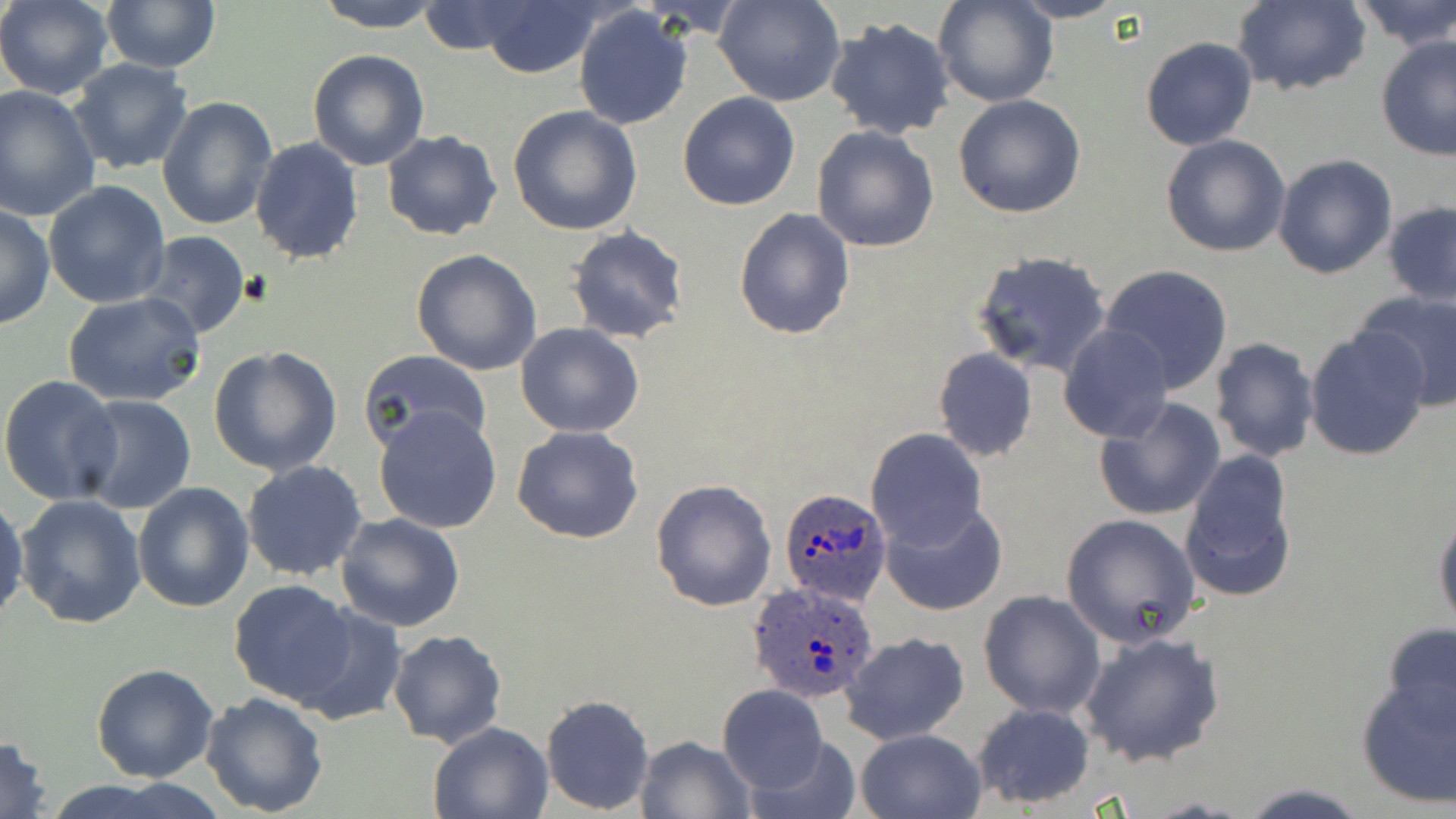
{
  "slide_level_diagnosis": "Plasmodium ovale",
  "image_size": "1456×819 pixels",
  "modality": "light microscopy",
  "field_of_view": "single",
  "magnification": "1000x",
  "preparation": "thin blood film",
  "stain": "May-Grünwald-Giemsa",
  "uninfected_red_blood_cell_locations": "approximate bounding boxes as [x1, y1, x2, y2] in pixels: [0, 0, 114, 99], [100, 0, 220, 72], [314, 0, 444, 32], [716, 0, 843, 106], [934, 0, 1055, 107], [1008, 0, 1126, 23], [1348, 0, 1456, 49], [473, 1, 604, 79], [1231, 1, 1370, 96], [418, 2, 525, 55], [572, 4, 693, 130], [824, 16, 956, 140], [1376, 33, 1456, 160], [1139, 37, 1258, 152], [307, 48, 430, 171], [68, 58, 193, 175], [0, 85, 101, 222], [677, 92, 801, 210], [953, 93, 1087, 218], [156, 95, 278, 232], [507, 104, 642, 234], [811, 124, 940, 254], [382, 130, 503, 241], [1160, 134, 1291, 258], [249, 137, 365, 265], [1272, 154, 1396, 279], [44, 182, 170, 308], [1383, 202, 1456, 306], [0, 204, 54, 331], [734, 207, 856, 340], [566, 226, 691, 344], [134, 232, 252, 340], [411, 249, 543, 376], [971, 250, 1111, 377], [1098, 264, 1237, 395], [1358, 289, 1456, 411], [63, 291, 206, 408], [515, 322, 645, 438], [1060, 324, 1174, 442], [1304, 327, 1431, 460], [1209, 337, 1319, 463], [209, 346, 343, 476], [933, 346, 1038, 462], [359, 349, 492, 456], [0, 375, 120, 505], [74, 395, 197, 513], [1094, 398, 1226, 523], [373, 404, 503, 533], [512, 426, 643, 544], [866, 429, 986, 552], [1178, 450, 1299, 602], [242, 460, 368, 582], [651, 478, 778, 612], [132, 482, 254, 613], [0, 492, 27, 625], [16, 494, 147, 629], [880, 500, 1007, 616], [1432, 505, 1456, 628], [335, 512, 465, 633], [1059, 513, 1203, 649], [229, 579, 359, 706], [978, 590, 1107, 718], [291, 602, 407, 724], [1381, 622, 1456, 733], [388, 629, 507, 748], [1078, 630, 1227, 767], [839, 631, 969, 746], [92, 664, 219, 783], [1356, 674, 1456, 808], [717, 685, 828, 794], [200, 691, 330, 815], [540, 694, 655, 816], [971, 702, 1097, 809], [428, 721, 555, 818], [855, 727, 987, 819], [634, 734, 756, 819], [0, 735, 54, 819], [745, 736, 863, 819], [1235, 782, 1373, 817]",
  "plasmodium_ovale_infected_red_blood_cell_locations": "approximate bounding boxes as [x1, y1, x2, y2] in pixels: [779, 488, 894, 608], [747, 579, 883, 702]"
}